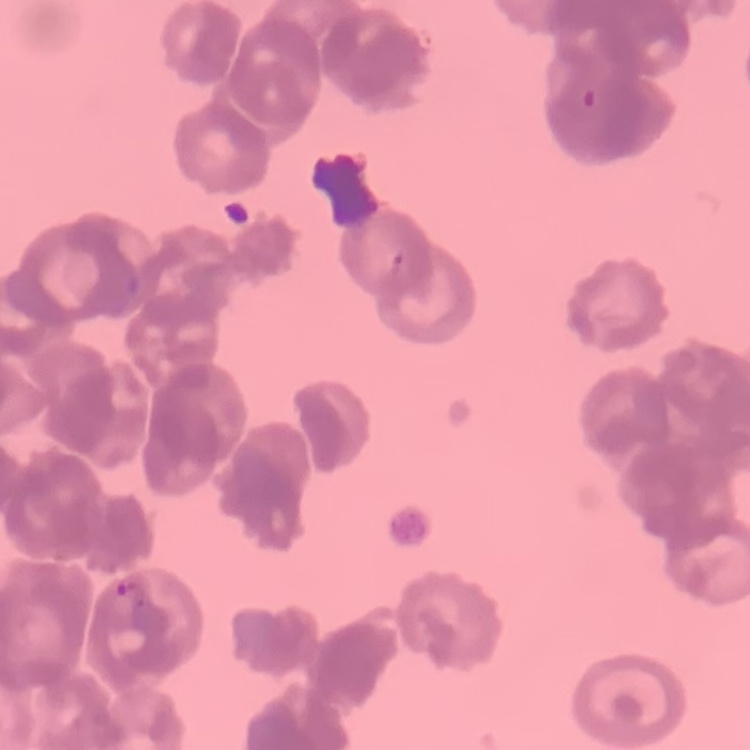

{
  "erythrocyte_morphology": "rouleaux formation",
  "image_type": "square crop of a larger photomicrograph",
  "preparation": "thin peripheral smear",
  "stain": "Field's or Giemsa"
}